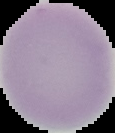
Cell region segmented out of the field of view; the surrounding area is masked to black. From a thin blood film. Result: no malaria parasites detected. Image is 115×133 pixels.